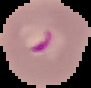

{
  "malaria_status": "parasitized",
  "image_size": "91×88 pixels",
  "image_type": "cell region segmented out of the field of view; surrounding area masked to black",
  "preparation": "thin blood film"
}